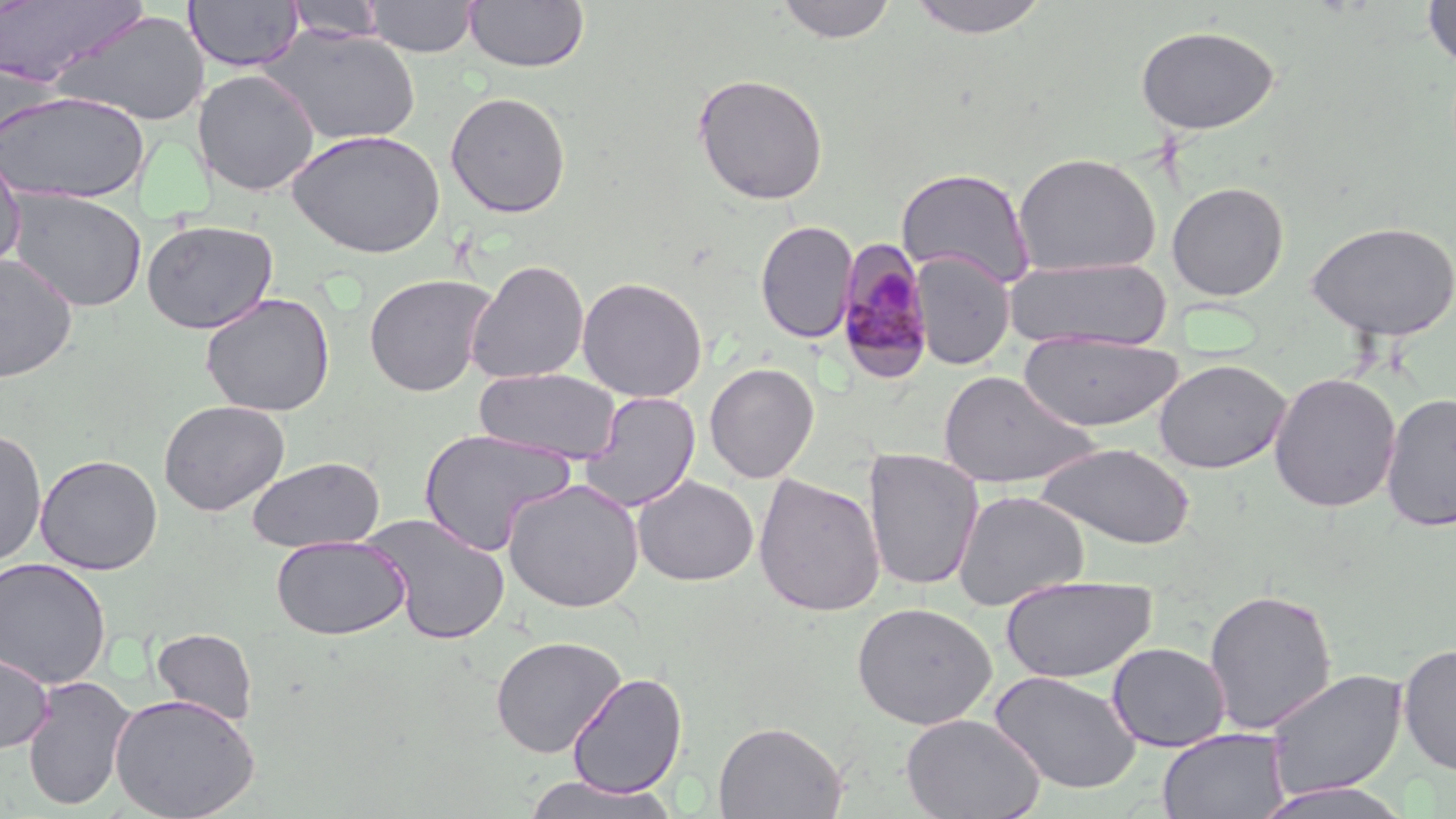

slide-level diagnosis = Plasmodium malariae
field of view = one of a larger specimen
modality = light microscopy
preparation = thin blood smear
Plasmodium malariae-infected red blood cell locations = approximate bounding boxes as (x1, y1, x2, y2) in pixels: (833, 240, 935, 382)
stain = May-Grünwald-Giemsa
uninfected red blood cell locations = approximate bounding boxes as (x1, y1, x2, y2) in pixels: (364, 0, 478, 57), (464, 0, 589, 73), (776, 0, 897, 44), (902, 0, 1054, 39), (1422, 0, 1455, 73), (0, 1, 149, 87), (184, 1, 303, 72), (286, 1, 387, 42), (53, 9, 210, 127), (1134, 25, 1281, 136), (259, 26, 422, 146), (192, 69, 321, 196), (692, 72, 829, 205), (0, 90, 151, 205), (445, 91, 572, 218), (286, 129, 447, 258), (0, 150, 26, 274), (1012, 152, 1161, 277), (895, 167, 1036, 288), (1167, 181, 1289, 301), (7, 187, 148, 312), (141, 219, 278, 334), (1305, 219, 1456, 341), (755, 220, 858, 343), (910, 252, 1014, 369), (0, 254, 77, 383), (1005, 257, 1172, 351), (465, 259, 590, 384), (364, 273, 496, 397), (576, 276, 708, 402), (200, 292, 336, 417), (1019, 331, 1184, 433), (1153, 358, 1291, 474), (704, 362, 820, 483), (474, 367, 622, 464), (937, 370, 1097, 489), (1268, 371, 1402, 513), (580, 392, 701, 512), (1380, 392, 1456, 532), (158, 399, 290, 516), (0, 428, 47, 569), (418, 428, 577, 556), (1036, 442, 1195, 550), (862, 449, 984, 592), (35, 454, 163, 575), (248, 456, 384, 553), (753, 473, 886, 617), (633, 475, 759, 586), (502, 478, 644, 612), (952, 490, 1089, 611), (363, 514, 512, 645), (271, 534, 410, 640), (0, 557, 112, 689), (1000, 574, 1158, 684), (1202, 587, 1337, 735), (852, 602, 997, 729), (152, 627, 258, 725), (490, 635, 626, 758), (1107, 641, 1231, 751), (1398, 643, 1456, 777), (0, 650, 55, 754), (1265, 668, 1408, 801), (989, 670, 1142, 794), (567, 672, 688, 798), (21, 675, 136, 811), (110, 693, 259, 818), (902, 713, 1045, 818), (713, 720, 847, 819), (1158, 728, 1289, 819), (519, 774, 679, 819), (1252, 782, 1416, 819)
magnification = 1000x
image size = 1456×819 pixels